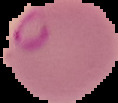

image type = segmented cell region with the area outside set to black
result = malaria parasites identified
preparation = thin blood film
image size = 118×103 pixels